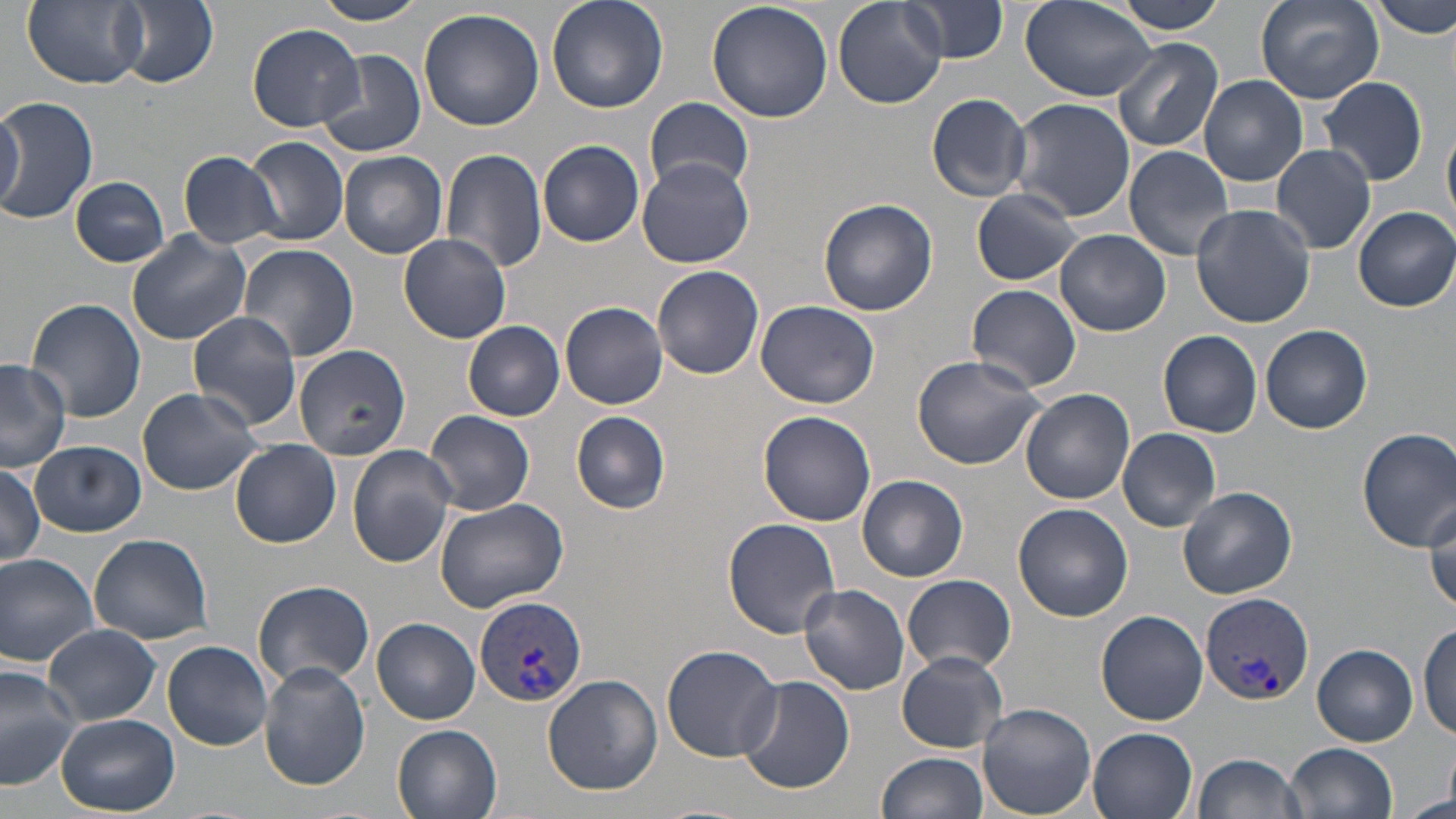
slide-level diagnosis = Plasmodium vivax
preparation = thin blood film
image size = 1456×819 pixels
magnification = 1000x
Plasmodium vivax-infected red blood cell locations = approximate bounding boxes as (x1, y1, x2, y2) in pixels: (1200, 591, 1313, 708), (475, 596, 587, 710)
field of view = one of a larger specimen
stain = May-Grünwald-Giemsa
uninfected red blood cell locations = approximate bounding boxes as (x1, y1, x2, y2) in pixels: (24, 0, 148, 89), (309, 0, 430, 26), (546, 0, 668, 113), (833, 0, 947, 110), (1112, 0, 1231, 33), (1253, 0, 1383, 102), (1373, 0, 1456, 39), (113, 1, 218, 87), (706, 1, 834, 122), (899, 1, 1011, 64), (1021, 1, 1156, 103), (418, 8, 545, 132), (248, 23, 366, 131), (1112, 37, 1224, 153), (314, 49, 427, 159), (1199, 74, 1307, 186), (1319, 75, 1429, 186), (926, 92, 1032, 201), (643, 96, 753, 199), (0, 97, 98, 225), (1008, 97, 1134, 221), (0, 104, 26, 211), (1443, 121, 1456, 229), (246, 136, 349, 246), (538, 140, 644, 247), (1271, 143, 1377, 255), (1123, 145, 1236, 260), (441, 148, 548, 274), (177, 150, 283, 248), (338, 150, 448, 258), (637, 158, 755, 269), (71, 176, 170, 267), (969, 188, 1083, 286), (818, 198, 938, 316), (1191, 203, 1315, 326), (1352, 205, 1456, 312), (1055, 229, 1171, 337), (126, 230, 256, 346), (398, 233, 512, 343), (236, 241, 359, 362), (652, 265, 764, 380), (966, 283, 1083, 393), (26, 298, 146, 424), (755, 299, 880, 409), (561, 301, 668, 409), (187, 313, 302, 431), (464, 320, 566, 420), (1260, 324, 1374, 434), (1157, 329, 1262, 437), (293, 343, 411, 460), (911, 353, 1046, 470), (0, 360, 71, 473), (137, 388, 263, 495), (1021, 388, 1135, 505), (425, 410, 534, 515), (571, 410, 671, 513), (758, 410, 877, 527), (1118, 427, 1222, 532), (1356, 428, 1456, 548), (231, 439, 341, 547), (30, 441, 146, 536), (347, 445, 459, 569), (383, 460, 513, 605), (0, 463, 46, 568), (857, 474, 968, 582), (1177, 485, 1297, 600), (433, 497, 569, 611), (1012, 503, 1133, 622), (1424, 504, 1455, 618), (724, 518, 844, 640), (88, 534, 213, 645), (0, 553, 100, 667), (900, 575, 1017, 674), (253, 579, 375, 688), (799, 584, 910, 694), (1097, 609, 1208, 725), (373, 618, 480, 724), (1416, 624, 1455, 740), (45, 625, 161, 726), (162, 639, 274, 749), (661, 643, 783, 762), (1313, 645, 1417, 745), (896, 651, 1009, 753), (258, 662, 371, 790), (0, 665, 82, 791), (734, 674, 855, 794), (543, 675, 663, 795), (978, 703, 1097, 819), (57, 713, 179, 815), (391, 722, 503, 819), (1087, 727, 1198, 819), (1286, 741, 1399, 819), (879, 751, 989, 819), (1191, 751, 1306, 819), (1400, 793, 1456, 818)
modality = optical microscopy